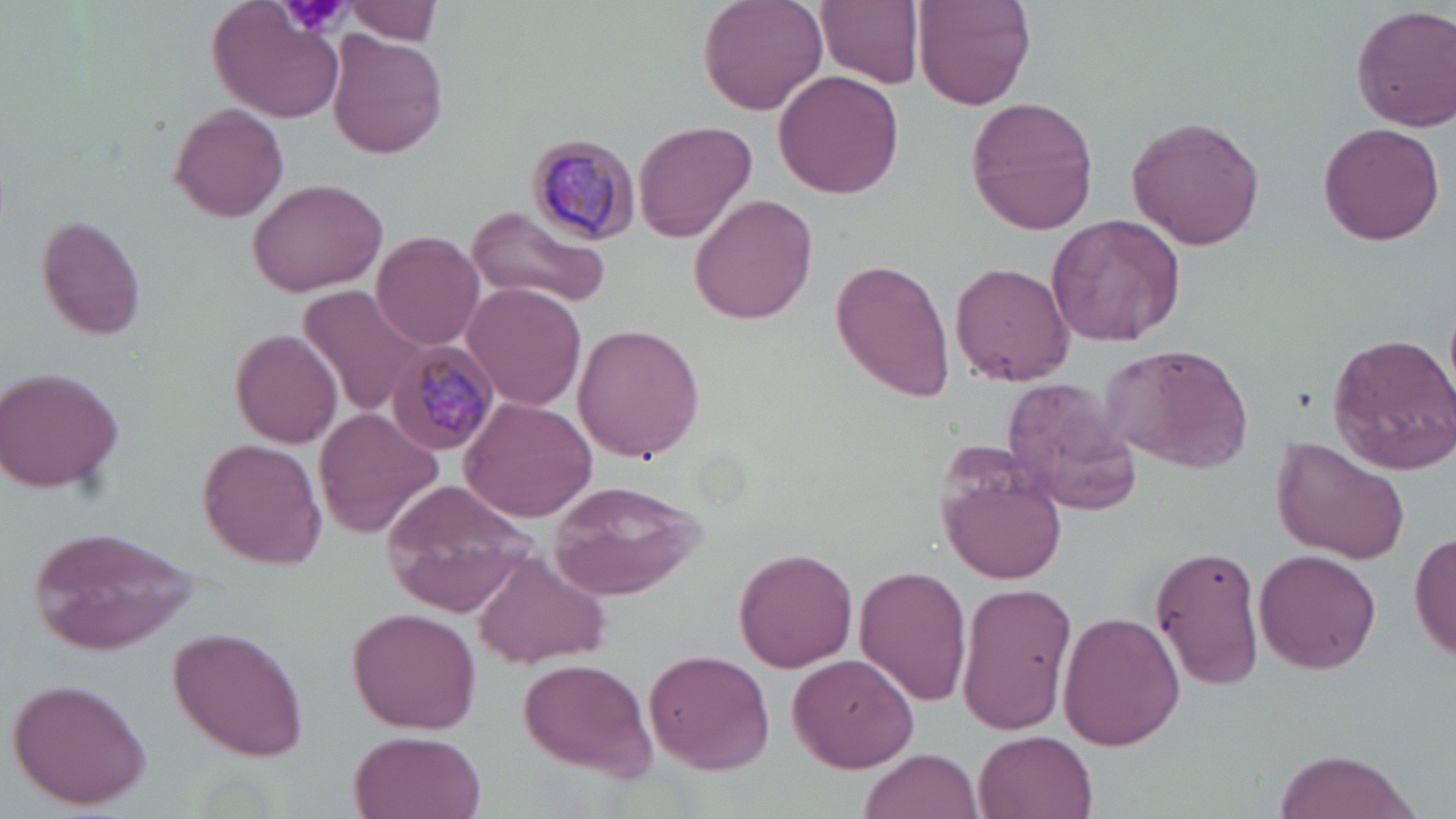

Approximate bounding boxes as (x1, y1, x2, y2) in pixels. Plasmodium malariae-infected red blood cell locations: (523, 131, 645, 246), (389, 345, 501, 457). Platelet locations: (279, 0, 352, 37). Uninfected red blood cell locations: (698, 0, 828, 115), (819, 0, 925, 87), (342, 1, 444, 44), (912, 1, 1036, 111), (209, 4, 348, 126), (1350, 4, 1456, 132), (330, 32, 449, 159), (774, 69, 905, 199), (965, 98, 1098, 231), (168, 105, 288, 221), (1126, 116, 1265, 250), (634, 120, 757, 243), (1318, 122, 1445, 245), (246, 175, 389, 296), (689, 193, 820, 324), (464, 206, 610, 308), (1048, 213, 1185, 347), (35, 216, 146, 341), (371, 233, 482, 349), (831, 256, 956, 401), (951, 262, 1073, 385), (462, 282, 586, 411), (297, 284, 431, 416), (573, 323, 707, 462), (228, 327, 343, 450), (1327, 331, 1456, 472), (1100, 343, 1256, 471), (0, 367, 127, 495), (1002, 381, 1142, 515), (460, 397, 597, 523), (314, 407, 443, 538), (1270, 437, 1410, 564), (199, 438, 329, 570), (939, 466, 1068, 588), (383, 479, 540, 617), (545, 479, 707, 599), (25, 527, 205, 655), (1409, 530, 1456, 663), (1150, 541, 1267, 690), (734, 547, 858, 672), (1254, 549, 1383, 677), (475, 553, 609, 669), (857, 566, 973, 705), (954, 580, 1078, 736), (1058, 609, 1185, 749), (350, 610, 479, 732), (170, 625, 312, 763), (644, 648, 775, 775), (788, 652, 917, 772), (517, 658, 660, 780), (7, 675, 153, 810), (349, 729, 485, 818), (973, 731, 1097, 819), (1271, 747, 1422, 819), (861, 748, 982, 818). Slide-level diagnosis: Plasmodium malariae. Optical microscopy. 1000x magnification. Thin blood film. Image is 1456×819 pixels. Single field of view. May-Grünwald-Giemsa stain.